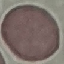

Result: no malaria parasites seen. Thin smear of blood. Acquired by smartphone through the microscope eyepiece. Cell patch, automatically extracted from a larger field of view and resized to 64 × 64 pixels. Giemsa-stained preparation.